Report the malaria status of this cell.
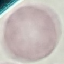
It is uninfected.

Giemsa-stained preparation. Acquired by smartphone through the microscope eyepiece. Thin blood film. Automatically extracted cell patch, resized to 64 × 64 pixels.